Classify this cell by malaria status.
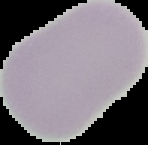
It is uninfected.

Summary:
  - Image size: 148×145 pixels
  - Preparation: thin blood film
  - Image type: segmented cell region with the area outside set to black